Describe the morphology of the erythrocytes.
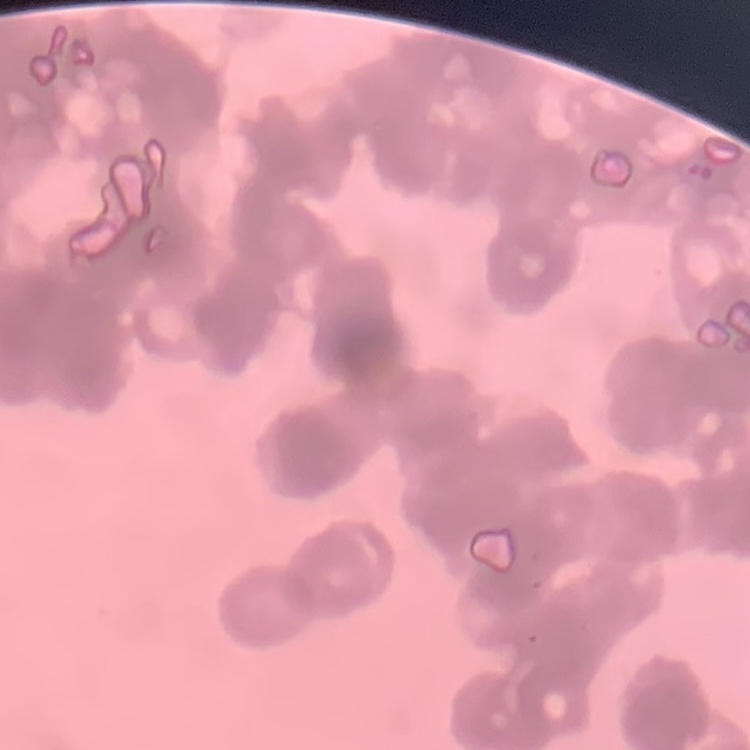
Rouleaux formation.

Summary:
  - Preparation: thin blood smear
  - Image type: square crop of a larger photomicrograph
  - Stain: Field's or Giemsa